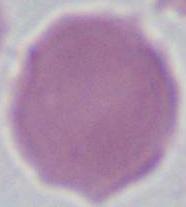
Micrograph. Captured at 1000x magnification. A red blood cell is shown.